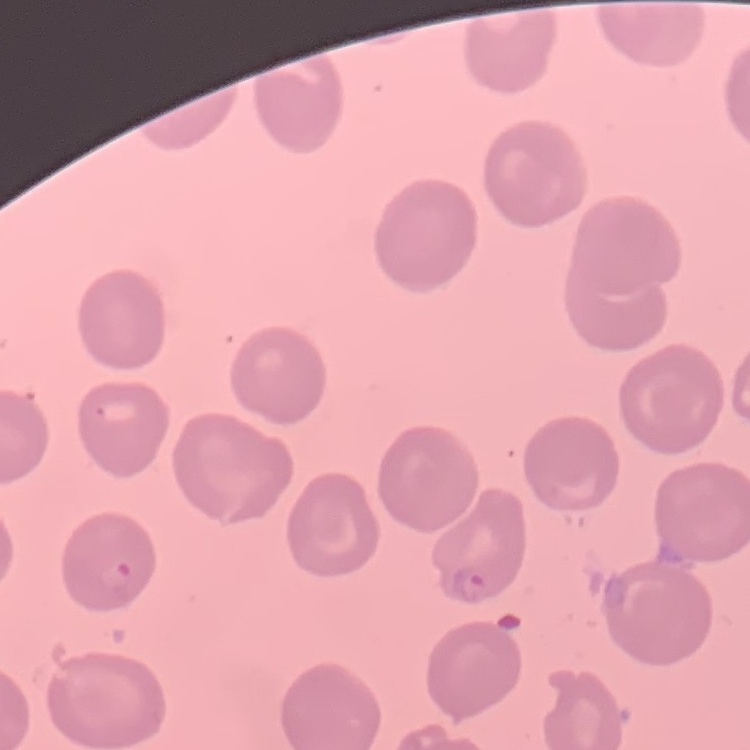 The red blood cells show no rouleaux formation. Thin blood smear. Field's or Giemsa stain. One tile cut from a larger photomicrograph.